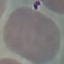

malaria status = uninfected
image type = cell patch, automatically extracted from a larger field of view and resized to 64 × 64 pixels
preparation = thin blood smear
stain = Giemsa
capture = smartphone through the microscope eyepiece